Point out each malaria parasite.
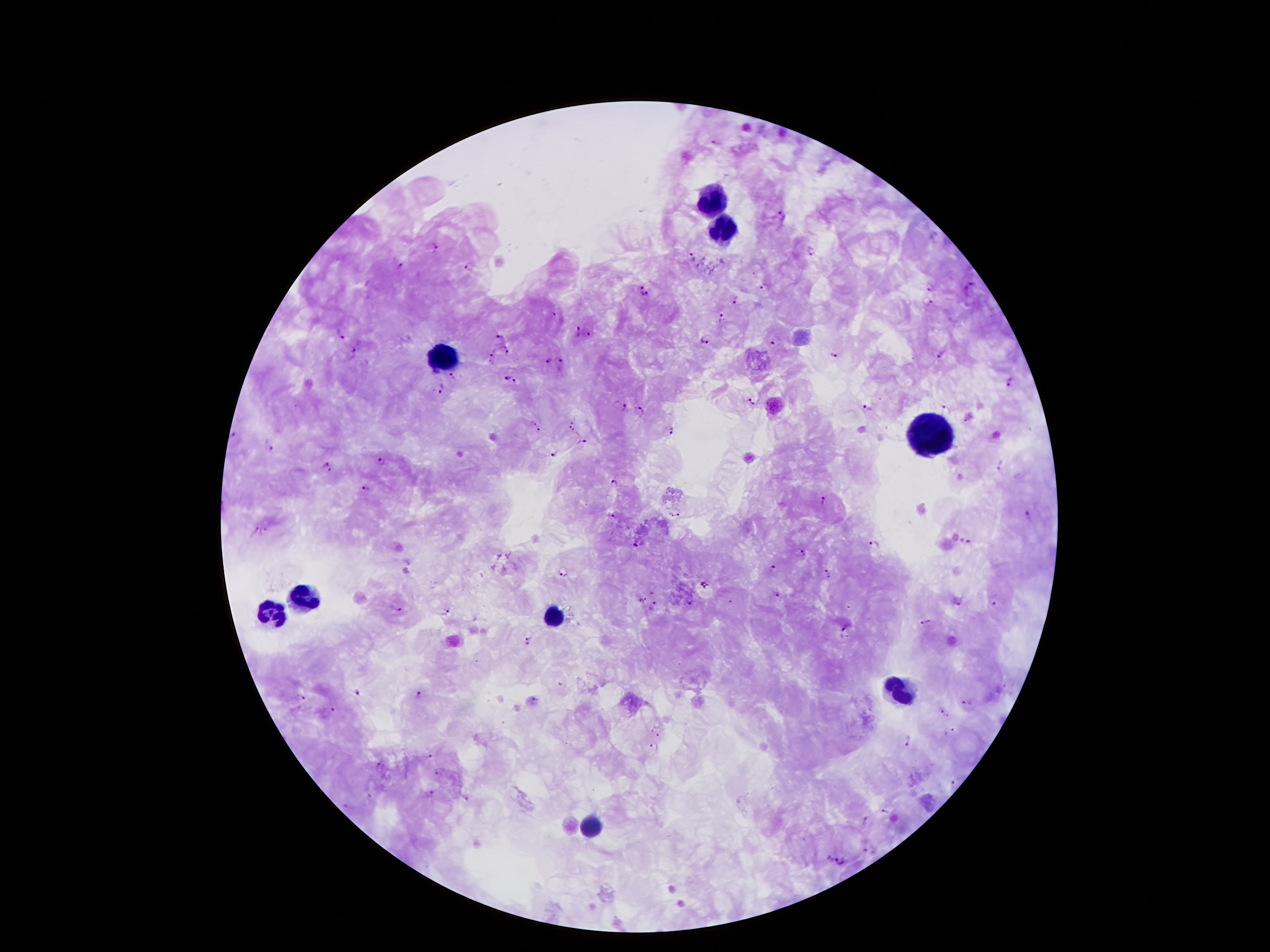
Approximate object centers, in pixels from the top-left corner.
Malaria parasites: (x=717, y=144), (x=782, y=215), (x=436, y=245), (x=810, y=250), (x=692, y=256), (x=401, y=264), (x=471, y=266), (x=642, y=284), (x=970, y=286), (x=765, y=287), (x=931, y=287), (x=645, y=295), (x=738, y=299), (x=931, y=301), (x=555, y=315), (x=723, y=318), (x=577, y=330), (x=340, y=333), (x=590, y=333), (x=501, y=336), (x=705, y=341), (x=776, y=341), (x=507, y=349), (x=355, y=350), (x=942, y=353), (x=835, y=354), (x=492, y=355), (x=548, y=360), (x=561, y=362), (x=454, y=375), (x=506, y=377), (x=1011, y=380), (x=516, y=382), (x=441, y=388), (x=752, y=400), (x=624, y=406), (x=948, y=408), (x=869, y=409), (x=641, y=410), (x=573, y=419), (x=531, y=421), (x=569, y=428), (x=541, y=430), (x=674, y=430), (x=234, y=433), (x=585, y=440), (x=270, y=442), (x=554, y=453), (x=382, y=461), (x=324, y=462), (x=1000, y=465), (x=331, y=472), (x=614, y=482), (x=366, y=488), (x=822, y=499), (x=613, y=515), (x=671, y=515), (x=680, y=515), (x=1028, y=515), (x=255, y=526), (x=265, y=530), (x=965, y=541), (x=639, y=544), (x=874, y=545), (x=800, y=551), (x=773, y=568), (x=826, y=568), (x=563, y=571), (x=830, y=579), (x=705, y=585), (x=777, y=594), (x=642, y=599), (x=691, y=601), (x=730, y=602), (x=958, y=602), (x=997, y=603), (x=397, y=606), (x=654, y=606), (x=449, y=609), (x=926, y=622), (x=844, y=626), (x=528, y=635), (x=527, y=647), (x=357, y=692), (x=419, y=693), (x=300, y=698), (x=535, y=700), (x=968, y=701), (x=332, y=708), (x=945, y=710), (x=652, y=728), (x=950, y=729), (x=662, y=735), (x=910, y=741), (x=653, y=747), (x=429, y=754), (x=381, y=764), (x=440, y=774), (x=954, y=783), (x=431, y=793), (x=370, y=796), (x=467, y=799), (x=345, y=807), (x=882, y=811), (x=866, y=820), (x=867, y=849), (x=830, y=858), (x=840, y=861).

Summary:
  - Leukocyte locations: (x=715, y=197), (x=721, y=226), (x=442, y=358), (x=933, y=433), (x=299, y=599), (x=551, y=617), (x=265, y=619), (x=899, y=692), (x=592, y=826)
  - Preparation: thick blood film
  - Field of view: single
  - Image size: 1270×952 pixels
  - Magnification: 100x
  - Stain: Giemsa
  - Patient malaria status: positive for Plasmodium falciparum
  - Capture: smartphone camera through the microscope eyepiece